Point out each Plasmodium parasite.
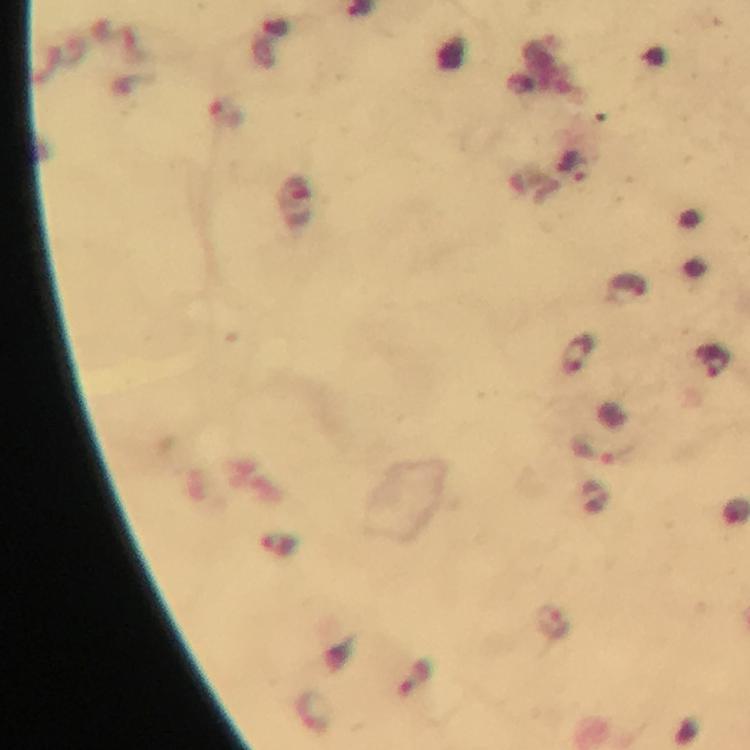
Approximate object centers, in pixels from the top-left corner.
Plasmodium parasites: (x=573, y=166), (x=575, y=353), (x=713, y=362), (x=604, y=451), (x=552, y=623).

{
  "immersion_oil": "applied",
  "image_size": "750×750 pixels",
  "stain": "Giemsa",
  "magnification": "100x",
  "capture": "smartphone mounted on the microscope",
  "context": "from a malaria diagnostic workup",
  "preparation": "thick blood film",
  "cropped_from": "a single field of view"
}